Classify this cell by malaria status.
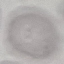
It is uninfected.

{
  "preparation": "thin smear",
  "stain": "Giemsa",
  "capture": "smartphone through the microscope eyepiece",
  "image_type": "automatically extracted cell patch, resized to 64 × 64 pixels"
}